Report the malaria status of this cell.
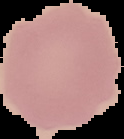

Uninfected.

preparation: thin blood smear
image_size: 124×139 pixels
image_type: cell region segmented out of the field of view; surrounding area masked to black